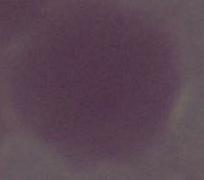
identification = erythrocyte
magnification = 1000x
modality = photomicrograph